State which cell type is depicted.
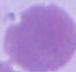

This is an erythrocyte.

magnification = 1000x
modality = micrograph